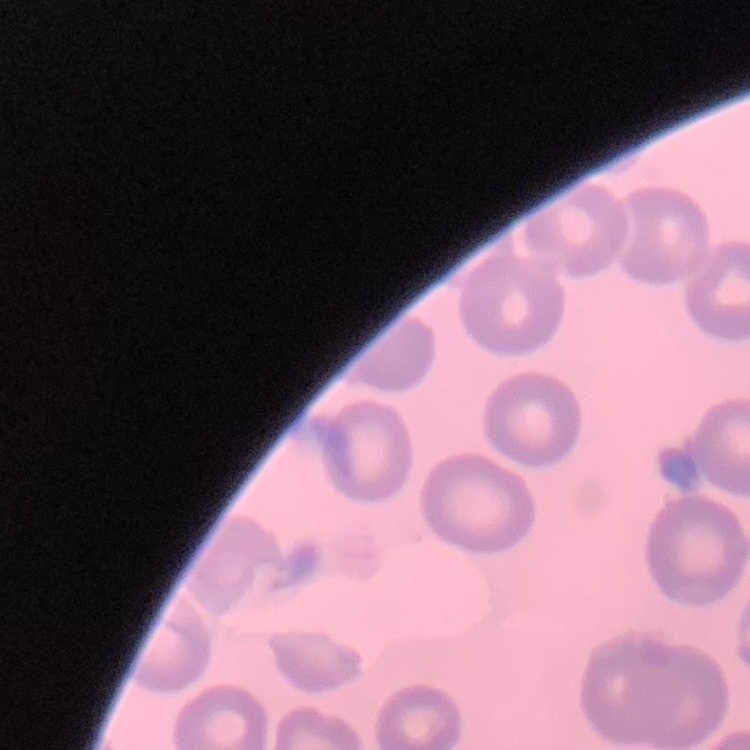
{
  "erythrocyte_morphology": "no rouleaux formation",
  "preparation": "thin blood smear",
  "stain": "Field's or Giemsa",
  "image_type": "square crop of a larger photomicrograph"
}